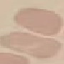
Summary:
  - Malaria status: uninfected
  - Preparation: thin smear
  - Stain: Giemsa
  - Image type: cell patch, automatically extracted from a larger field of view and resized to 64 × 64 pixels
  - Capture: smartphone through the microscope eyepiece